Assess this cell for malaria.
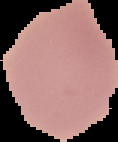

Uninfected.

From a thin blood smear. Segmented cell region on a black background. Image is 118×142 pixels.